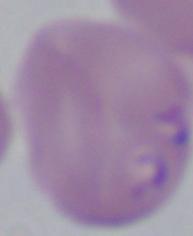 Photomicrograph. Captured at 1000x magnification. A Babesia parasite is seen.